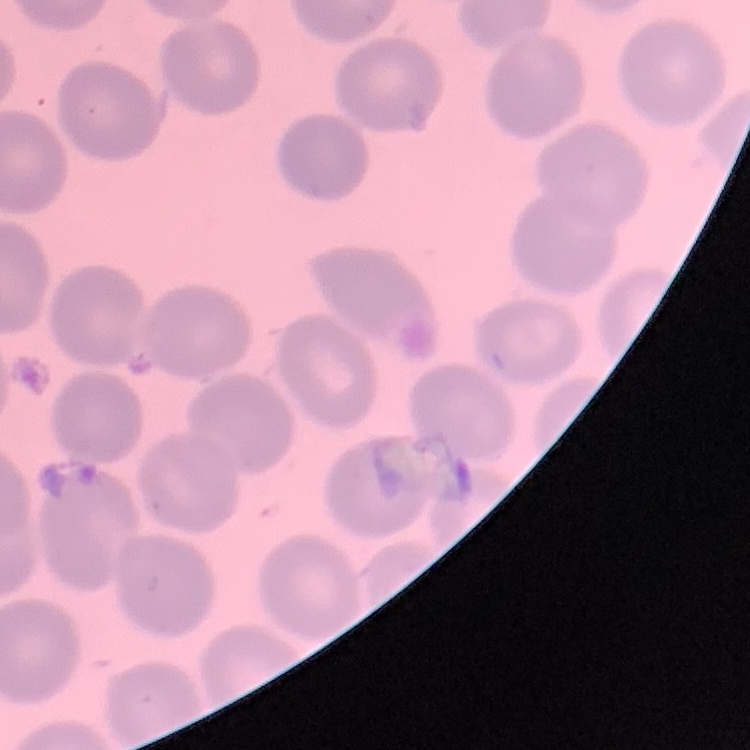

erythrocyte morphology = no rouleaux formation
stain = Field's or Giemsa
preparation = thin peripheral smear
image type = square crop of a larger photomicrograph